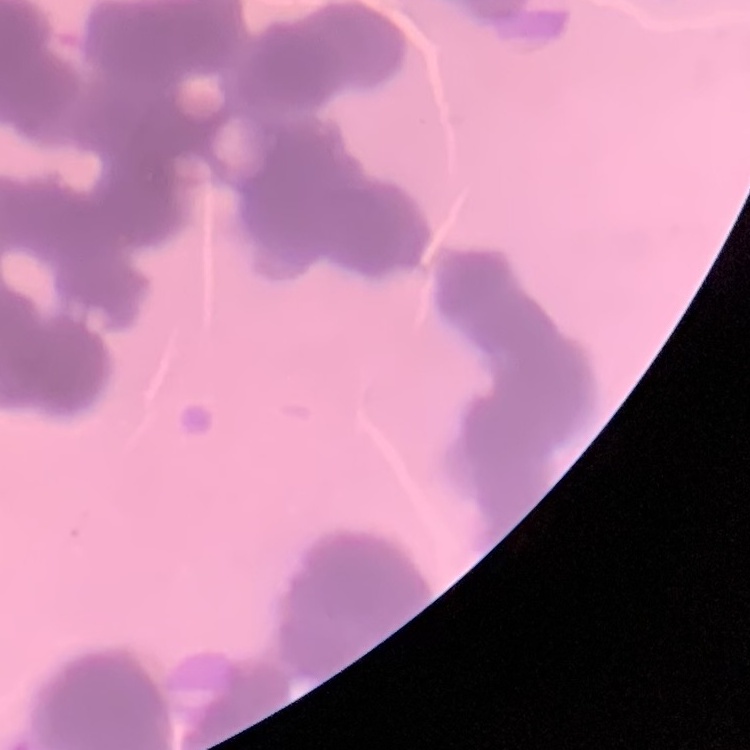

The erythrocytes show rouleaux formation. Stained with either Field's or Giemsa. Thin blood smear. Square crop of a larger photomicrograph.